Identify the parasite.
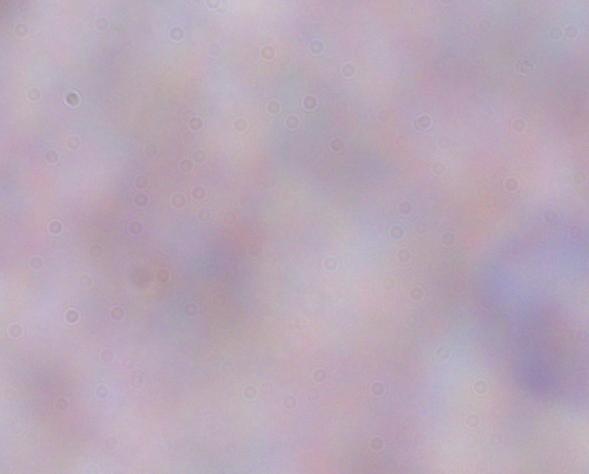

This is a trypanosome.

1000x magnification. Photomicrograph.